Locate and identify every blood parasite.
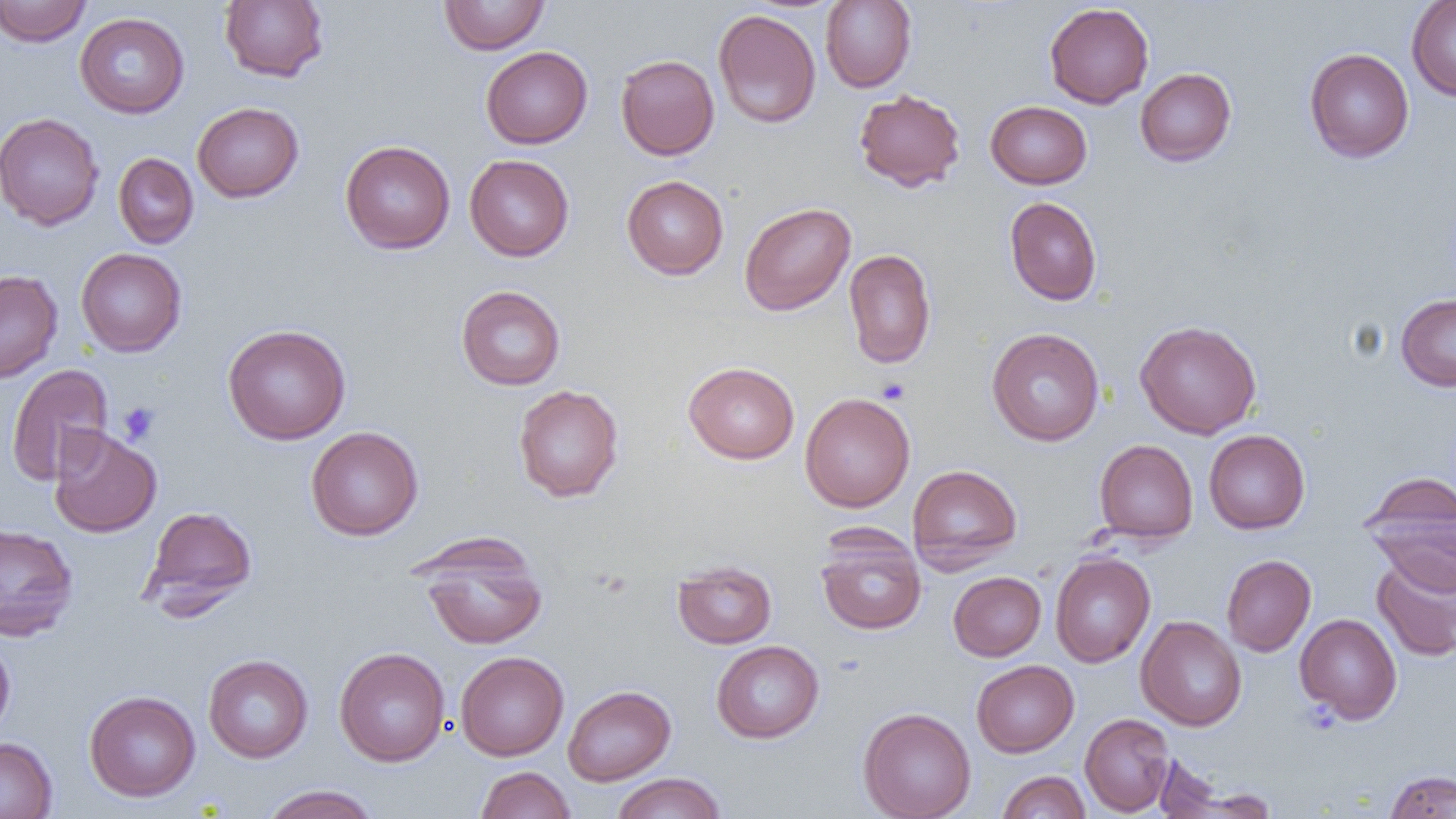

No blood parasites seen.

slide_level_diagnosis: negative for blood parasites
modality: light microscopy
platelet_locations: 'approximate bounding boxes as [x1, y1, x2, y2] in pixels: [877, 378, 911, 405], [117, 402, 161, 445], [1299, 699, 1342, 735]'
field_of_view: single
magnification: 1000x
preparation: thin blood smear
image_size: 1456×819 pixels
uninfected_red_blood_cell_locations: 'approximate bounding boxes as [x1, y1, x2, y2] in pixels: [0, 0, 92, 47], [219, 0, 329, 83], [438, 0, 550, 55], [820, 1, 916, 92], [1407, 1, 1456, 101], [713, 3, 917, 99], [1044, 3, 1154, 108], [713, 8, 821, 128], [75, 12, 189, 118], [481, 46, 593, 148], [1304, 48, 1414, 163], [615, 54, 719, 160], [1135, 68, 1236, 166], [853, 88, 966, 192], [986, 101, 1092, 189], [192, 102, 304, 202], [0, 112, 104, 230], [340, 140, 455, 254], [113, 153, 198, 249], [464, 154, 574, 261], [622, 175, 729, 279], [1004, 196, 1102, 305], [739, 202, 856, 316], [75, 248, 187, 357], [843, 248, 936, 368], [0, 270, 62, 383], [456, 285, 566, 390], [1395, 293, 1456, 391], [1135, 320, 1261, 439], [222, 324, 351, 445], [987, 328, 1104, 446], [683, 361, 800, 464], [5, 363, 114, 486], [513, 384, 624, 502], [799, 392, 915, 512], [48, 425, 162, 538], [306, 426, 423, 541], [1203, 429, 1310, 534], [1094, 439, 1198, 544], [907, 464, 1022, 571], [1360, 473, 1455, 592], [141, 505, 258, 613], [0, 522, 78, 641], [815, 530, 927, 635], [417, 536, 547, 651], [1050, 552, 1155, 667], [1222, 554, 1316, 656], [1371, 554, 1456, 662], [672, 560, 776, 649], [948, 571, 1046, 660], [1294, 613, 1402, 724], [1136, 616, 1246, 731], [0, 636, 15, 740], [711, 640, 824, 743], [334, 647, 450, 767], [455, 651, 569, 761], [203, 654, 314, 763], [971, 660, 1079, 757], [562, 685, 676, 786], [84, 690, 201, 801], [858, 707, 976, 819], [1080, 713, 1174, 816], [0, 736, 58, 819], [1149, 757, 1261, 816], [475, 766, 575, 819], [1384, 769, 1456, 818], [996, 771, 1091, 818], [611, 772, 726, 818], [259, 784, 381, 819]'